Identify the preparation type.
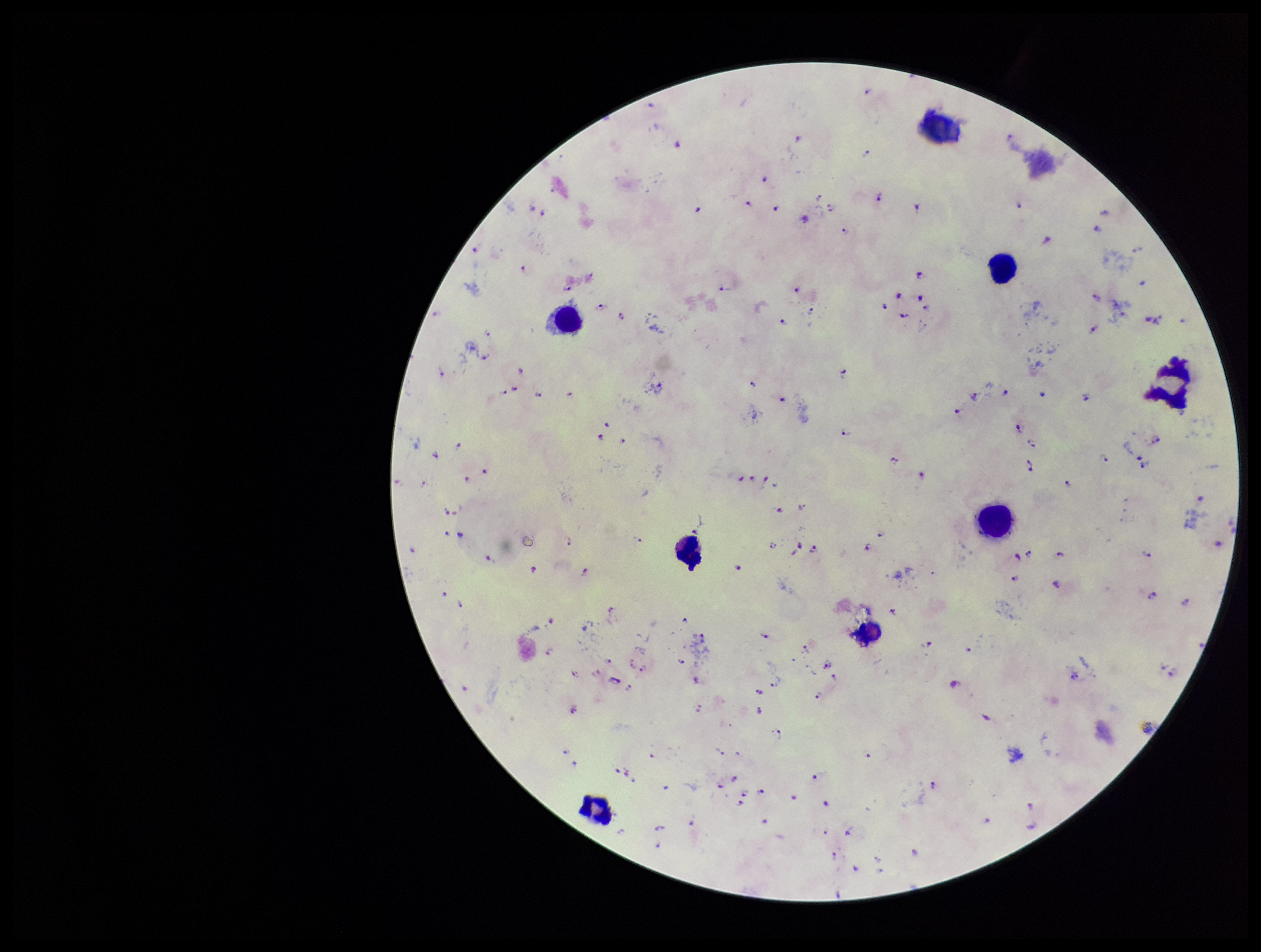
It is a thick blood smear.

Summary:
  - Species reported for this patient: Plasmodium falciparum
  - Field of view: single
  - Plasmodium parasites: seen
  - Parasite count: 123
  - Stain: Giemsa
  - Leukocyte count: 8
  - Patient malaria status: infected
  - Image size: 1261×952 pixels
  - Capture: smartphone photograph through the microscope eyepiece